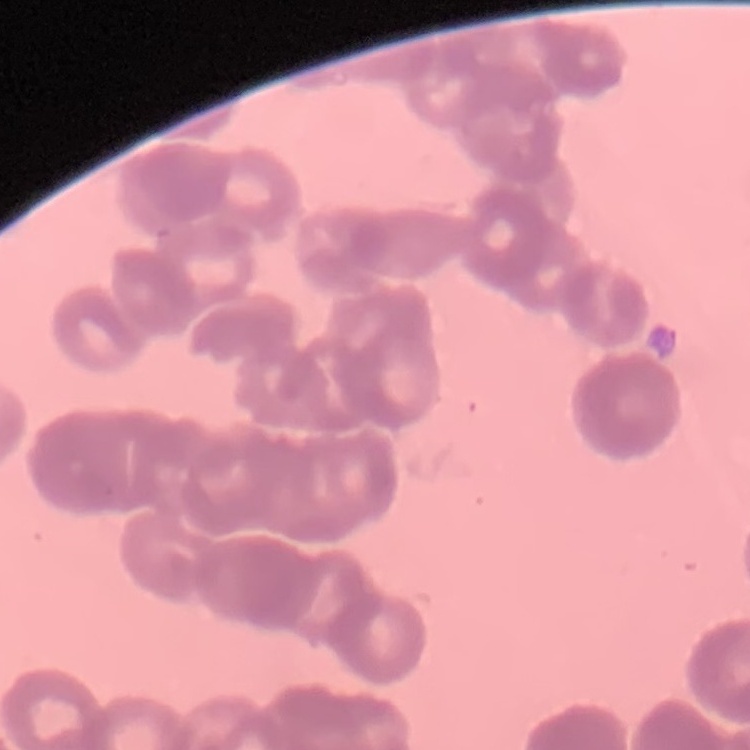 The erythrocytes exhibit rouleaux formation. Thin blood film. Square crop of a larger photomicrograph. Stained with either Field's or Giemsa.